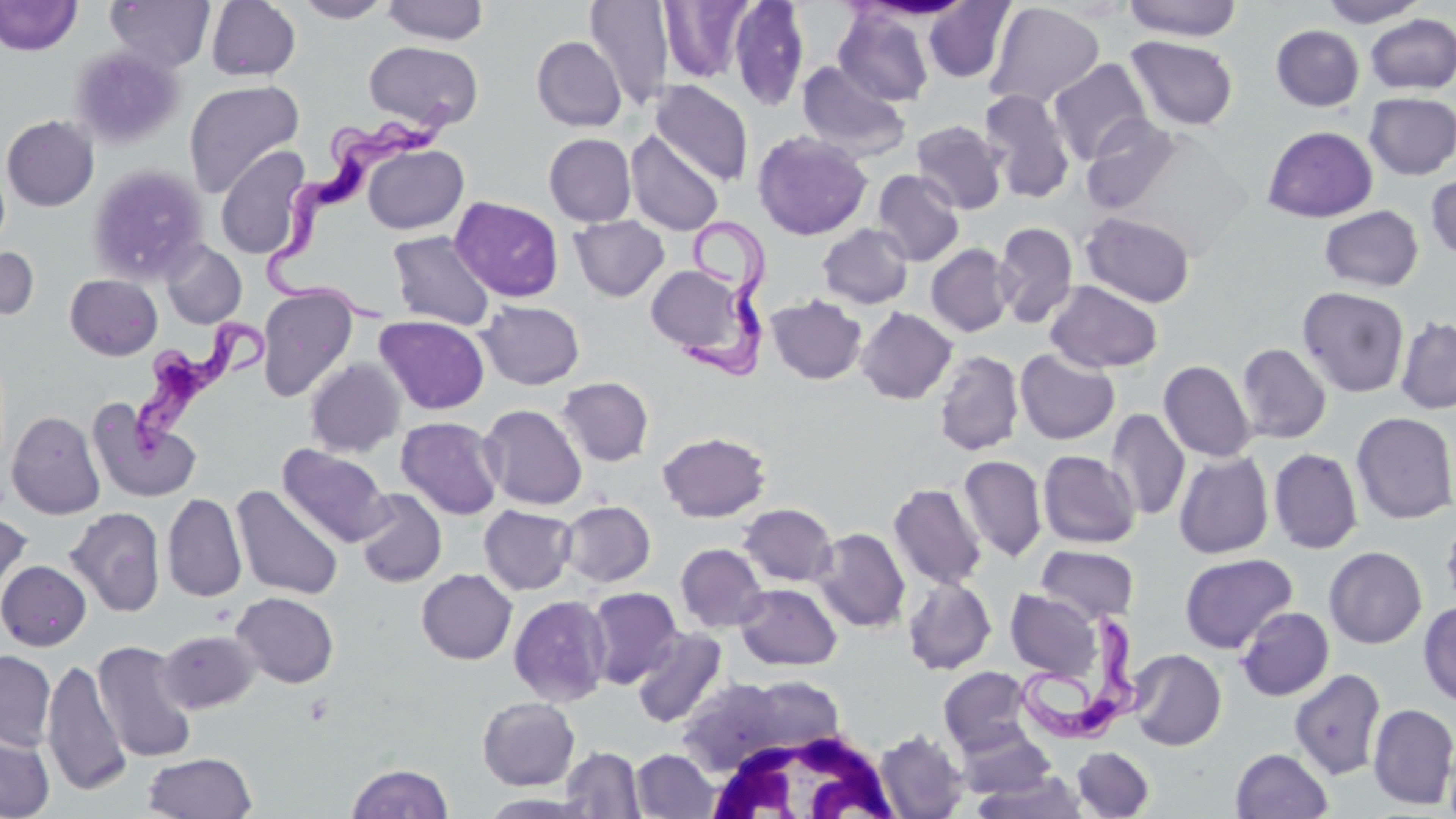

Approximate bounding boxes as (x1, y1, x2, y2) in pixels. White blood cell locations: (696, 723, 903, 819). Uninfected red blood cell locations: (0, 0, 81, 56), (105, 0, 216, 72), (206, 0, 301, 81), (293, 0, 396, 23), (382, 0, 489, 45), (728, 0, 810, 110), (923, 0, 1016, 84), (1123, 0, 1242, 40), (1319, 0, 1428, 27), (584, 1, 674, 109), (659, 1, 755, 84), (984, 2, 1104, 109), (833, 7, 934, 106), (1365, 14, 1456, 95), (1271, 24, 1364, 111), (531, 36, 626, 132), (1125, 36, 1239, 131), (363, 41, 484, 131), (68, 44, 186, 149), (1048, 58, 1152, 165), (797, 61, 911, 161), (184, 79, 305, 197), (651, 80, 753, 186), (979, 90, 1076, 203), (1363, 91, 1456, 180), (1, 115, 99, 212), (1081, 116, 1182, 214), (911, 120, 1007, 215), (1262, 125, 1378, 222), (626, 129, 724, 236), (752, 130, 872, 240), (544, 133, 636, 226), (364, 144, 468, 234), (215, 147, 310, 259), (86, 163, 209, 284), (872, 169, 965, 267), (1425, 172, 1456, 262), (450, 196, 564, 302), (1319, 205, 1423, 292), (1081, 211, 1196, 307), (570, 216, 669, 301), (993, 221, 1078, 328), (817, 224, 913, 309), (387, 231, 496, 331), (161, 241, 246, 329), (926, 243, 1014, 337), (0, 245, 39, 322), (645, 264, 754, 360), (65, 274, 162, 360), (1045, 280, 1163, 373), (257, 286, 358, 402), (1297, 286, 1410, 398), (767, 295, 867, 384), (478, 300, 584, 390), (856, 307, 957, 404), (375, 315, 489, 414), (1395, 316, 1456, 414), (1236, 343, 1332, 444), (1015, 348, 1119, 444), (934, 350, 1024, 456), (1024, 350, 1125, 549), (305, 359, 405, 457), (1159, 360, 1256, 462), (557, 376, 654, 466), (87, 399, 201, 502), (480, 404, 587, 510), (1106, 409, 1189, 520), (6, 410, 106, 519), (1351, 411, 1456, 524), (396, 416, 504, 520), (657, 431, 770, 522), (277, 445, 391, 547), (1268, 448, 1363, 554), (1038, 450, 1141, 548), (1174, 451, 1273, 559), (958, 455, 1047, 562), (888, 482, 987, 590), (233, 485, 343, 600), (354, 489, 447, 587), (162, 492, 247, 603), (559, 500, 655, 587), (738, 503, 838, 587), (479, 504, 577, 595), (64, 506, 166, 617), (0, 512, 33, 607), (1441, 515, 1456, 611), (811, 527, 910, 632), (675, 543, 768, 632), (1036, 545, 1139, 623), (1324, 546, 1427, 649), (1179, 553, 1298, 654), (0, 560, 91, 651), (416, 568, 517, 664), (902, 577, 996, 675), (735, 583, 842, 670), (586, 587, 682, 688), (1005, 589, 1104, 680), (231, 591, 339, 688), (509, 595, 612, 706), (1418, 602, 1456, 707), (1236, 606, 1334, 700), (630, 627, 727, 728), (158, 630, 260, 713), (93, 639, 197, 763), (0, 649, 56, 751), (1127, 649, 1226, 750), (41, 658, 131, 797), (938, 667, 1034, 756), (1289, 668, 1386, 780), (677, 675, 836, 778), (477, 696, 580, 790), (1368, 703, 1456, 809), (955, 727, 1057, 799), (0, 729, 55, 818), (874, 729, 969, 818), (560, 746, 645, 818), (1071, 746, 1155, 819), (1230, 748, 1333, 819), (632, 749, 719, 818), (143, 752, 257, 819), (346, 763, 454, 818), (972, 771, 1090, 818). Trypanosoma brucei locations: (261, 96, 461, 324), (677, 214, 767, 380), (126, 313, 268, 463), (1019, 611, 1146, 747). Slide-level diagnosis: Trypanosoma brucei. Thin blood film. 1000x magnification. Single field of view. Light microscopy. May-Grünwald-Giemsa-stained preparation. Image is 1456×819 pixels.